Give the position of every leukocyte visible.
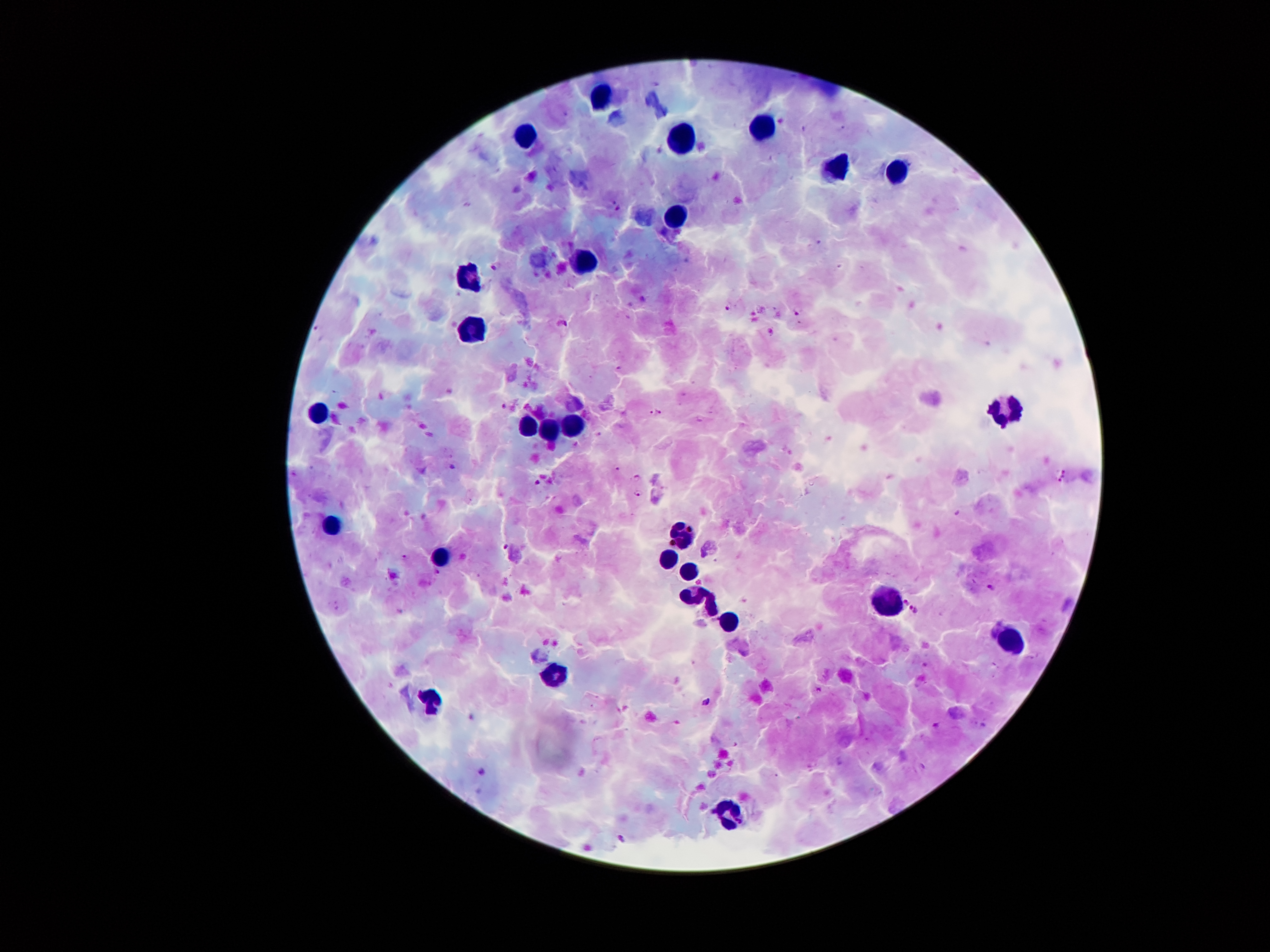
Approximate centers as (x, y) in pixels.
Leukocytes: (602, 99), (767, 127), (532, 136), (684, 139), (839, 169), (899, 169), (674, 218), (577, 260), (477, 277), (472, 325), (1009, 403), (321, 416), (336, 525), (686, 536), (672, 558), (687, 572), (690, 595), (889, 604), (711, 607), (729, 622), (1012, 641), (556, 672), (435, 697), (725, 812).

{
  "image_size": "1270×952 pixels",
  "magnification": "100x",
  "capture": "smartphone through the microscope eyepiece",
  "field_of_view": "single",
  "preparation": "thick blood film",
  "malaria_parasite_locations": "approximate centers as (x, y) in pixels: (494, 265), (727, 307), (797, 312), (563, 323), (504, 406), (659, 410), (651, 412), (453, 466), (619, 469), (636, 476), (537, 482), (637, 492), (505, 547), (406, 557), (437, 571), (992, 587), (905, 600), (910, 607), (917, 612), (818, 689), (706, 701)",
  "stain": "Giemsa",
  "patient_malaria_status": "positive for Plasmodium falciparum"
}